Report the malaria status of this cell.
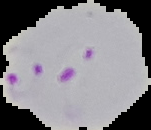

It is parasitized.

From a thin blood smear. Image is 151×130 pixels. Cell region segmented out of the field of view; the surrounding area is masked to black.